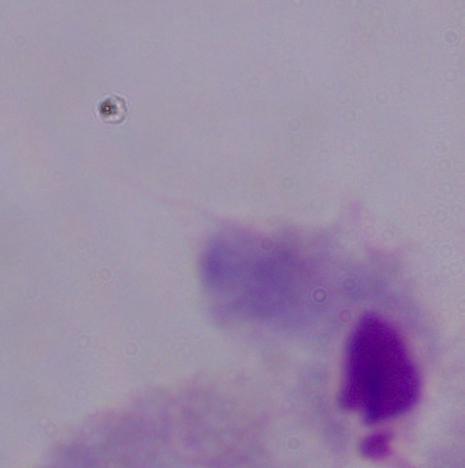

A trichomonad is shown. Captured at 1000x magnification. Photomicrograph.